Locate and identify every blood parasite.
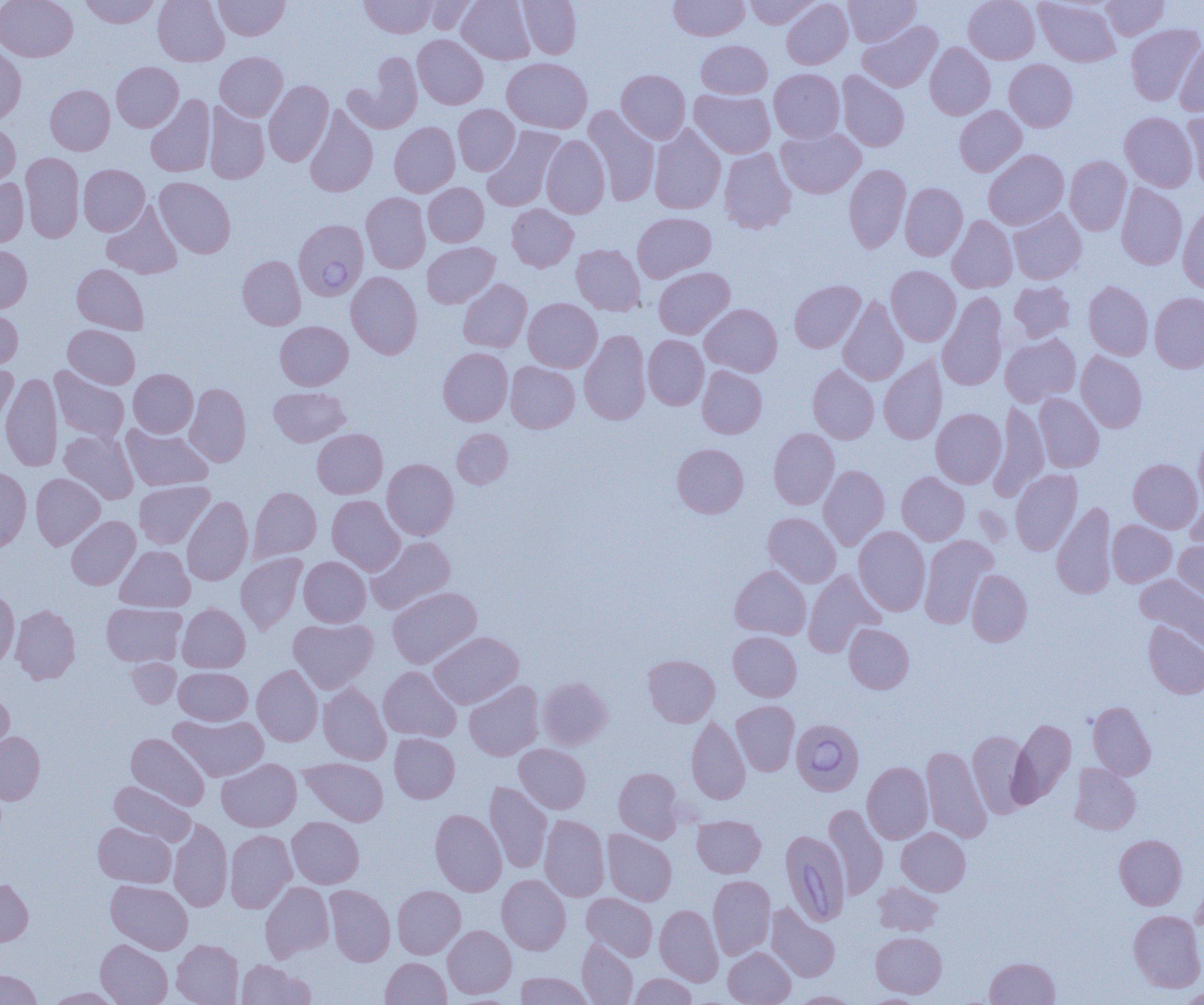

Approximate bounding boxes as named x1/y1/x2/y2 corners in pixels.
Babesia divergens-infected red blood cells: (x1=293, y1=219, x2=369, y2=300), (x1=791, y1=719, x2=864, y2=795), (x1=780, y1=830, x2=851, y2=926).
No Plasmodium falciparum, Plasmodium ovale, Plasmodium malariae, Plasmodium vivax, or Trypanosoma brucei observed.

slide-level diagnosis = Babesia divergens
magnification = 1000x
uninfected red blood cell locations = approximate bounding boxes as named x1/y1/x2/y2 corners in pixels: (x1=0, y1=0, x2=77, y2=61), (x1=79, y1=0, x2=161, y2=28), (x1=153, y1=0, x2=229, y2=66), (x1=360, y1=0, x2=436, y2=38), (x1=420, y1=0, x2=479, y2=34), (x1=457, y1=0, x2=535, y2=64), (x1=518, y1=0, x2=581, y2=59), (x1=669, y1=0, x2=750, y2=40), (x1=744, y1=0, x2=820, y2=29), (x1=781, y1=0, x2=853, y2=69), (x1=843, y1=0, x2=920, y2=47), (x1=964, y1=0, x2=1039, y2=64), (x1=1035, y1=0, x2=1119, y2=67), (x1=1101, y1=0, x2=1169, y2=39), (x1=214, y1=1, x2=290, y2=40), (x1=858, y1=21, x2=942, y2=92), (x1=1126, y1=24, x2=1203, y2=106), (x1=413, y1=35, x2=488, y2=109), (x1=696, y1=40, x2=772, y2=98), (x1=1175, y1=40, x2=1204, y2=115), (x1=925, y1=43, x2=995, y2=119), (x1=0, y1=46, x2=26, y2=124), (x1=215, y1=52, x2=287, y2=121), (x1=344, y1=55, x2=423, y2=134), (x1=501, y1=57, x2=592, y2=133), (x1=1004, y1=59, x2=1077, y2=132), (x1=112, y1=62, x2=183, y2=131), (x1=769, y1=68, x2=845, y2=143), (x1=616, y1=69, x2=691, y2=143), (x1=836, y1=71, x2=910, y2=152), (x1=264, y1=81, x2=334, y2=166), (x1=45, y1=85, x2=114, y2=155), (x1=689, y1=89, x2=775, y2=158), (x1=145, y1=94, x2=215, y2=177), (x1=204, y1=103, x2=269, y2=184), (x1=453, y1=104, x2=519, y2=175), (x1=304, y1=105, x2=378, y2=197), (x1=583, y1=105, x2=659, y2=206), (x1=955, y1=106, x2=1026, y2=176), (x1=1183, y1=110, x2=1204, y2=191), (x1=1120, y1=112, x2=1198, y2=192), (x1=0, y1=120, x2=20, y2=191), (x1=389, y1=122, x2=460, y2=197), (x1=649, y1=125, x2=726, y2=214), (x1=482, y1=126, x2=564, y2=212), (x1=776, y1=128, x2=866, y2=198), (x1=541, y1=135, x2=610, y2=218), (x1=719, y1=149, x2=796, y2=233), (x1=984, y1=149, x2=1069, y2=230), (x1=20, y1=152, x2=84, y2=243), (x1=1064, y1=156, x2=1131, y2=235), (x1=844, y1=164, x2=911, y2=253), (x1=78, y1=165, x2=150, y2=235), (x1=154, y1=177, x2=235, y2=258), (x1=0, y1=178, x2=29, y2=247), (x1=423, y1=183, x2=489, y2=247), (x1=900, y1=183, x2=968, y2=261), (x1=1116, y1=183, x2=1187, y2=269), (x1=361, y1=192, x2=430, y2=273), (x1=102, y1=202, x2=182, y2=279), (x1=506, y1=204, x2=578, y2=271), (x1=1177, y1=204, x2=1204, y2=293), (x1=1008, y1=209, x2=1086, y2=284), (x1=632, y1=212, x2=716, y2=282), (x1=947, y1=215, x2=1017, y2=293), (x1=422, y1=242, x2=500, y2=308), (x1=571, y1=244, x2=646, y2=315), (x1=0, y1=245, x2=31, y2=312), (x1=237, y1=255, x2=306, y2=330), (x1=72, y1=264, x2=149, y2=334), (x1=886, y1=266, x2=960, y2=346), (x1=653, y1=267, x2=735, y2=339), (x1=346, y1=271, x2=422, y2=359), (x1=458, y1=278, x2=532, y2=352), (x1=789, y1=280, x2=865, y2=352), (x1=1009, y1=281, x2=1075, y2=342), (x1=1083, y1=281, x2=1153, y2=360), (x1=1149, y1=292, x2=1204, y2=372), (x1=937, y1=293, x2=1008, y2=390), (x1=838, y1=296, x2=908, y2=386), (x1=523, y1=298, x2=602, y2=372), (x1=700, y1=304, x2=782, y2=376), (x1=0, y1=307, x2=23, y2=370), (x1=275, y1=321, x2=353, y2=390), (x1=63, y1=324, x2=140, y2=389), (x1=579, y1=329, x2=651, y2=425), (x1=1000, y1=333, x2=1081, y2=407), (x1=643, y1=335, x2=709, y2=410), (x1=438, y1=348, x2=513, y2=426), (x1=1076, y1=351, x2=1147, y2=432), (x1=879, y1=356, x2=947, y2=444), (x1=505, y1=361, x2=580, y2=433), (x1=0, y1=363, x2=18, y2=427), (x1=808, y1=365, x2=879, y2=444), (x1=697, y1=366, x2=767, y2=438), (x1=50, y1=367, x2=129, y2=442), (x1=129, y1=369, x2=198, y2=437), (x1=0, y1=373, x2=62, y2=471), (x1=185, y1=383, x2=251, y2=466), (x1=269, y1=386, x2=350, y2=446), (x1=1034, y1=393, x2=1104, y2=472), (x1=989, y1=400, x2=1048, y2=500), (x1=931, y1=408, x2=1006, y2=488), (x1=122, y1=424, x2=212, y2=491), (x1=452, y1=428, x2=513, y2=488), (x1=768, y1=428, x2=839, y2=510), (x1=312, y1=429, x2=387, y2=498), (x1=1194, y1=429, x2=1204, y2=509), (x1=59, y1=430, x2=138, y2=504), (x1=672, y1=443, x2=749, y2=518), (x1=1128, y1=458, x2=1202, y2=533), (x1=382, y1=459, x2=458, y2=540), (x1=819, y1=465, x2=889, y2=549), (x1=0, y1=466, x2=31, y2=553), (x1=1010, y1=469, x2=1082, y2=555), (x1=897, y1=471, x2=969, y2=545), (x1=31, y1=473, x2=105, y2=549), (x1=134, y1=480, x2=214, y2=548), (x1=249, y1=487, x2=322, y2=561), (x1=327, y1=495, x2=404, y2=575), (x1=1186, y1=496, x2=1204, y2=558), (x1=182, y1=497, x2=253, y2=585), (x1=1052, y1=502, x2=1117, y2=599), (x1=763, y1=512, x2=841, y2=587), (x1=66, y1=516, x2=140, y2=589), (x1=1108, y1=520, x2=1176, y2=586), (x1=853, y1=527, x2=931, y2=616), (x1=367, y1=535, x2=456, y2=614), (x1=919, y1=535, x2=997, y2=628), (x1=1174, y1=539, x2=1204, y2=603), (x1=115, y1=545, x2=194, y2=612), (x1=236, y1=553, x2=307, y2=633), (x1=299, y1=557, x2=370, y2=627), (x1=730, y1=565, x2=811, y2=639), (x1=803, y1=569, x2=885, y2=658), (x1=966, y1=569, x2=1032, y2=646), (x1=1135, y1=574, x2=1204, y2=649), (x1=387, y1=587, x2=482, y2=668), (x1=0, y1=590, x2=19, y2=668), (x1=102, y1=603, x2=186, y2=667), (x1=177, y1=603, x2=250, y2=672), (x1=11, y1=604, x2=80, y2=685), (x1=288, y1=618, x2=378, y2=692), (x1=1143, y1=620, x2=1204, y2=699), (x1=844, y1=623, x2=914, y2=694), (x1=429, y1=631, x2=523, y2=709), (x1=728, y1=631, x2=801, y2=701), (x1=643, y1=654, x2=720, y2=727), (x1=126, y1=658, x2=181, y2=708), (x1=252, y1=665, x2=323, y2=746), (x1=173, y1=666, x2=322, y2=733), (x1=378, y1=666, x2=461, y2=742), (x1=175, y1=667, x2=252, y2=725), (x1=538, y1=676, x2=612, y2=749), (x1=464, y1=680, x2=544, y2=761), (x1=318, y1=683, x2=391, y2=765), (x1=0, y1=688, x2=14, y2=764), (x1=731, y1=700, x2=800, y2=775), (x1=1088, y1=701, x2=1156, y2=779), (x1=169, y1=714, x2=268, y2=781), (x1=687, y1=716, x2=750, y2=804), (x1=1009, y1=718, x2=1076, y2=807), (x1=968, y1=730, x2=1033, y2=817), (x1=0, y1=732, x2=45, y2=804), (x1=126, y1=733, x2=210, y2=810), (x1=389, y1=733, x2=460, y2=803), (x1=514, y1=744, x2=590, y2=814), (x1=921, y1=745, x2=992, y2=843), (x1=217, y1=758, x2=301, y2=831), (x1=299, y1=758, x2=389, y2=825), (x1=862, y1=761, x2=933, y2=844), (x1=1069, y1=763, x2=1141, y2=835), (x1=614, y1=767, x2=684, y2=842), (x1=109, y1=781, x2=195, y2=846), (x1=485, y1=782, x2=552, y2=873), (x1=824, y1=804, x2=888, y2=899), (x1=430, y1=809, x2=506, y2=896), (x1=539, y1=815, x2=610, y2=902), (x1=692, y1=815, x2=766, y2=877), (x1=287, y1=816, x2=364, y2=888), (x1=168, y1=818, x2=232, y2=911), (x1=93, y1=821, x2=176, y2=888), (x1=897, y1=828, x2=971, y2=895), (x1=225, y1=830, x2=297, y2=913), (x1=602, y1=830, x2=677, y2=905), (x1=1114, y1=834, x2=1187, y2=910), (x1=497, y1=874, x2=570, y2=954), (x1=708, y1=875, x2=775, y2=960), (x1=0, y1=878, x2=33, y2=946), (x1=106, y1=880, x2=193, y2=954), (x1=873, y1=881, x2=943, y2=936), (x1=260, y1=882, x2=334, y2=961), (x1=325, y1=885, x2=395, y2=966), (x1=392, y1=885, x2=465, y2=958), (x1=581, y1=893, x2=657, y2=960), (x1=766, y1=904, x2=840, y2=982), (x1=655, y1=905, x2=723, y2=985), (x1=1129, y1=910, x2=1204, y2=992), (x1=443, y1=925, x2=516, y2=998), (x1=872, y1=932, x2=947, y2=998), (x1=96, y1=939, x2=172, y2=1005), (x1=172, y1=939, x2=243, y2=1005), (x1=577, y1=939, x2=638, y2=1004), (x1=723, y1=947, x2=796, y2=1005), (x1=381, y1=957, x2=451, y2=1005), (x1=985, y1=957, x2=1060, y2=1004), (x1=236, y1=959, x2=314, y2=1005), (x1=0, y1=970, x2=42, y2=1005), (x1=515, y1=971, x2=593, y2=1004), (x1=629, y1=973, x2=697, y2=1004), (x1=45, y1=987, x2=124, y2=1004), (x1=1178, y1=988, x2=1204, y2=1004), (x1=792, y1=991, x2=858, y2=1004), (x1=864, y1=993, x2=930, y2=1004)
image size = 1204×1005 pixels
modality = light microscopy
field of view = one of a larger specimen
preparation = thin blood film